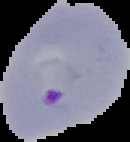
image size = 130×142 pixels
image type = segmented cell region on a black background
preparation = thin blood film
malaria status = parasitized